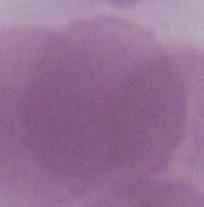

An erythrocyte is seen. Captured at 1000x magnification. Photomicrograph.